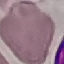
Summary:
  - Result: negative for malaria parasites
  - Preparation: thin blood smear
  - Capture: smartphone through the microscope eyepiece
  - Stain: Giemsa
  - Image type: cell patch, automatically extracted from a larger field of view and resized to 64 × 64 pixels